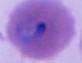
magnification: 400x or 1000x
identification: Plasmodium
modality: photomicrograph